Report the malaria status of this cell.
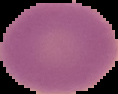
Uninfected.

{
  "image_size": "118×94 pixels",
  "preparation": "thin blood smear",
  "image_type": "segmented cell region on a black background"
}